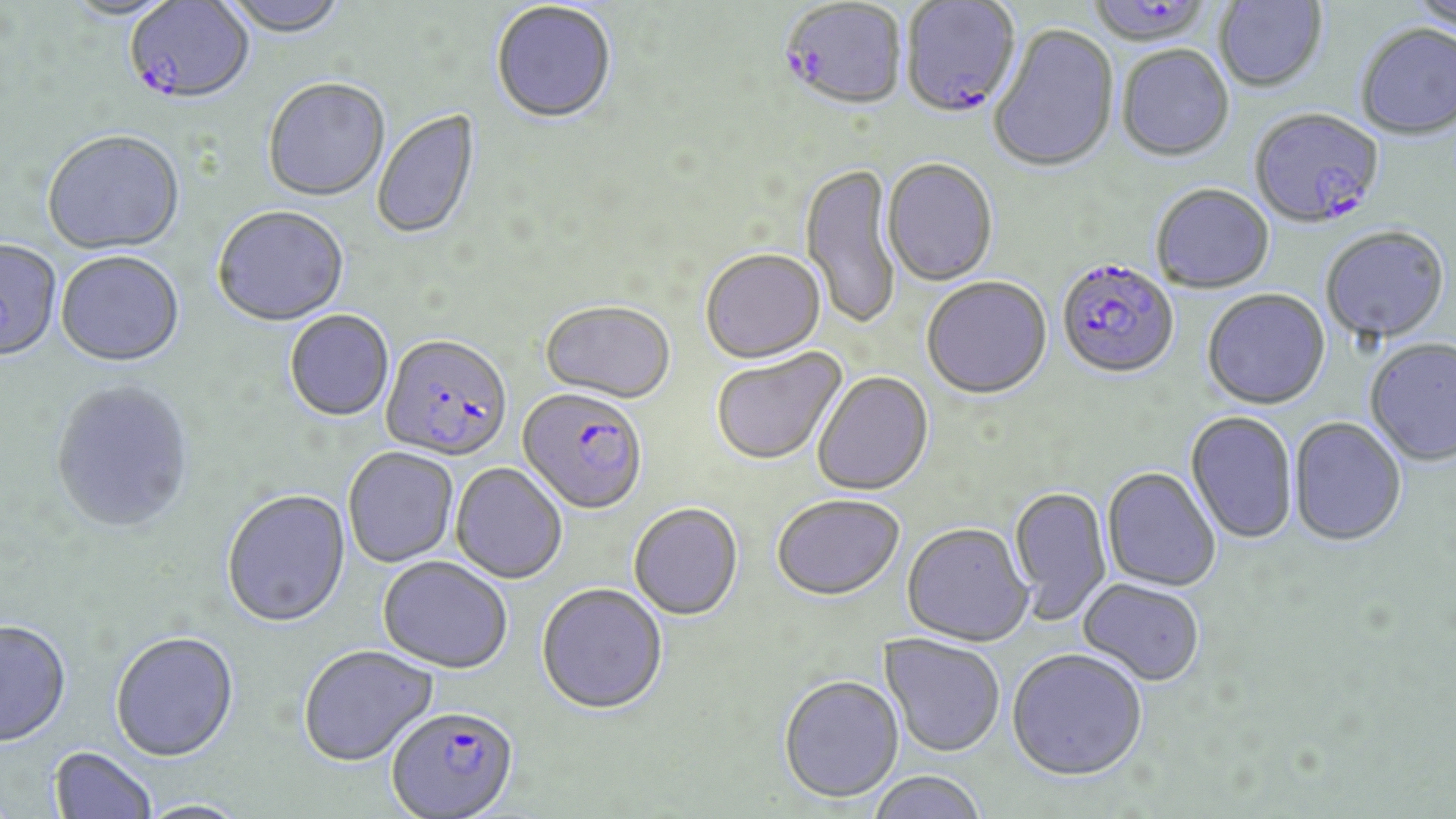

Summary:
  - Coordinate format: approximate bounding boxes as named x1/y1/x2/y2 corners in pixels
  - Plasmodium falciparum-infected red blood cell locations: (x1=899, y1=0, x2=1022, y2=117), (x1=1090, y1=0, x2=1215, y2=47), (x1=779, y1=1, x2=907, y2=111), (x1=129, y1=2, x2=256, y2=105), (x1=1250, y1=107, x2=1384, y2=229), (x1=1056, y1=258, x2=1179, y2=379), (x1=381, y1=334, x2=512, y2=464), (x1=518, y1=386, x2=648, y2=514), (x1=387, y1=706, x2=518, y2=818)
  - Uninfected red blood cell locations: (x1=60, y1=0, x2=185, y2=23), (x1=221, y1=0, x2=350, y2=39), (x1=1409, y1=0, x2=1456, y2=34), (x1=1213, y1=1, x2=1328, y2=92), (x1=490, y1=3, x2=617, y2=126), (x1=1355, y1=23, x2=1456, y2=139), (x1=989, y1=24, x2=1119, y2=174), (x1=1116, y1=46, x2=1234, y2=162), (x1=263, y1=79, x2=390, y2=203), (x1=372, y1=110, x2=481, y2=242), (x1=42, y1=133, x2=185, y2=257), (x1=882, y1=159, x2=998, y2=286), (x1=800, y1=162, x2=902, y2=331), (x1=1151, y1=184, x2=1275, y2=294), (x1=212, y1=207, x2=349, y2=328), (x1=1320, y1=225, x2=1450, y2=344), (x1=0, y1=241, x2=61, y2=365), (x1=700, y1=249, x2=825, y2=363), (x1=55, y1=253, x2=184, y2=369), (x1=921, y1=276, x2=1052, y2=400), (x1=1202, y1=289, x2=1331, y2=410), (x1=540, y1=300, x2=676, y2=403), (x1=284, y1=310, x2=394, y2=422), (x1=1365, y1=337, x2=1456, y2=467), (x1=710, y1=348, x2=846, y2=466), (x1=812, y1=370, x2=933, y2=496), (x1=50, y1=381, x2=194, y2=535), (x1=1186, y1=412, x2=1298, y2=544), (x1=1288, y1=417, x2=1407, y2=546), (x1=343, y1=447, x2=459, y2=568), (x1=451, y1=462, x2=568, y2=584), (x1=1102, y1=467, x2=1221, y2=592), (x1=1009, y1=484, x2=1112, y2=626), (x1=221, y1=489, x2=351, y2=629), (x1=771, y1=493, x2=904, y2=600), (x1=629, y1=502, x2=744, y2=620), (x1=902, y1=522, x2=1033, y2=646), (x1=378, y1=557, x2=513, y2=673), (x1=1077, y1=578, x2=1206, y2=686), (x1=536, y1=583, x2=668, y2=715), (x1=0, y1=622, x2=72, y2=750), (x1=110, y1=633, x2=240, y2=764), (x1=879, y1=633, x2=1006, y2=757), (x1=298, y1=645, x2=439, y2=768), (x1=1007, y1=647, x2=1147, y2=780), (x1=778, y1=674, x2=905, y2=802), (x1=50, y1=748, x2=157, y2=819), (x1=866, y1=771, x2=989, y2=819), (x1=134, y1=800, x2=252, y2=819)
  - Slide-level diagnosis: Plasmodium falciparum
  - Modality: light microscopy
  - Image size: 1456×819 pixels
  - Preparation: thin blood smear
  - Magnification: 1000x
  - Stain: May-Grünwald-Giemsa
  - Field of view: one of a larger specimen